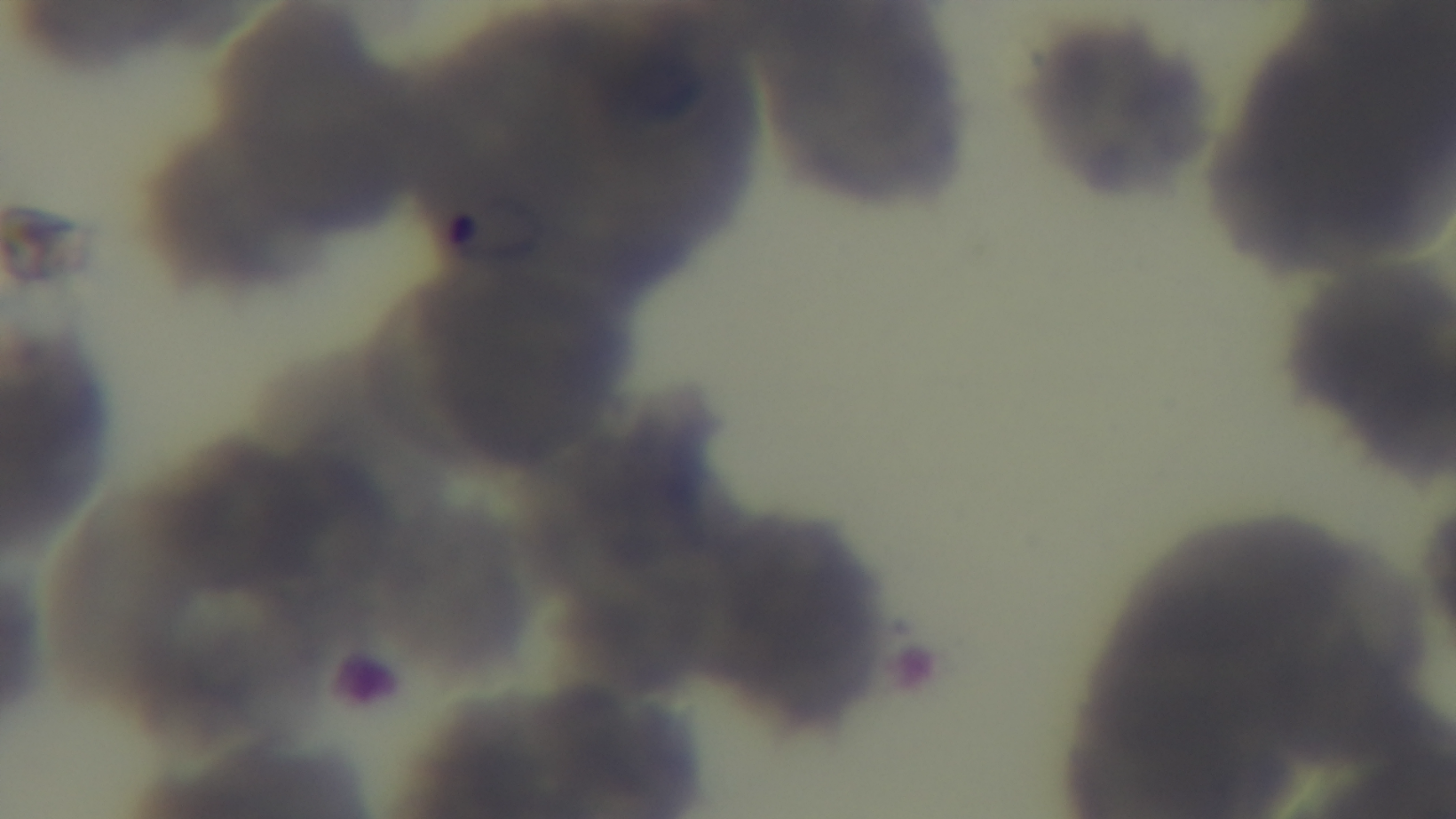

Single field of view. Photomicrograph. 100x oil-immersion objective. Mounted 4K digital camera. Giemsa stain. Preparation: thin smear. Malaria status: infected.